Comment on the morphology of the erythrocytes.
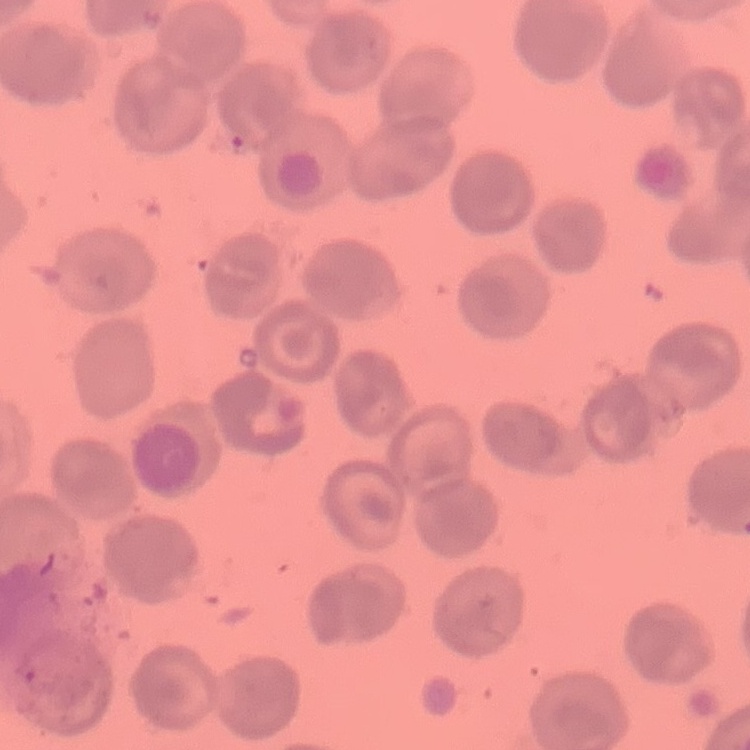
They show no rouleaux formation.

image_type: one tile cut from a larger photomicrograph
preparation: thin blood film
stain: Field's or Giemsa